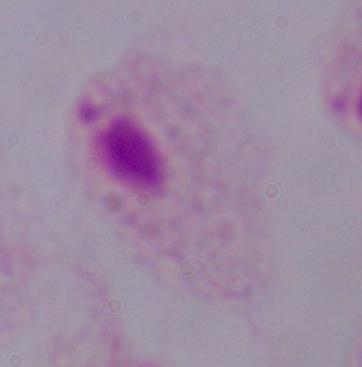

Micrograph. Captured at 1000x magnification. A trichomonad is seen.